Assess the morphology of the erythrocytes.
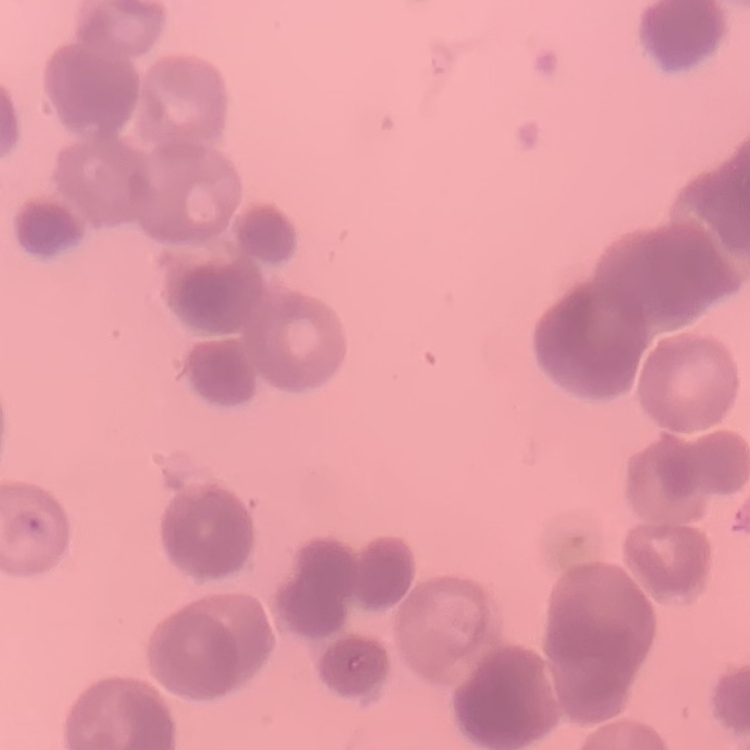

Rouleaux formation.

Summary:
  - Preparation: thin blood film
  - Stain: Field's or Giemsa
  - Image type: one tile cut from a larger photomicrograph